Classify this cell by malaria status.
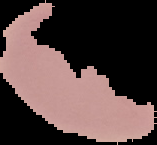

It is uninfected.

Segmented cell region on a black background. From a thin blood film. Image is 157×145 pixels.